Name the parasite shown.
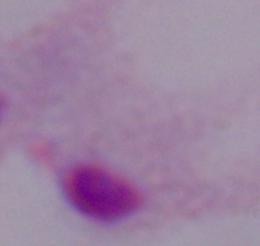
A trichomonad.

Captured at 1000x magnification. Micrograph.